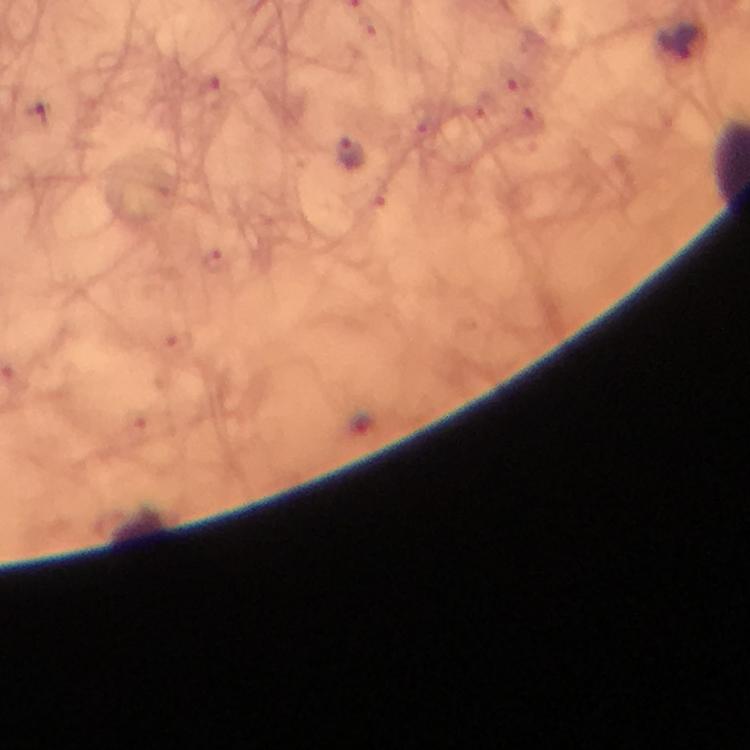

preparation = thick blood film
context = from a diagnostic examination for malaria
immersion oil = used
magnification = 100x
capture = smartphone mounted on the microscope
Plasmodium parasite locations = approximate centers as (x, y) in pixels: (680, 43), (350, 156)
cropped from = one field of view
image size = 750×750 pixels
stain = Giemsa